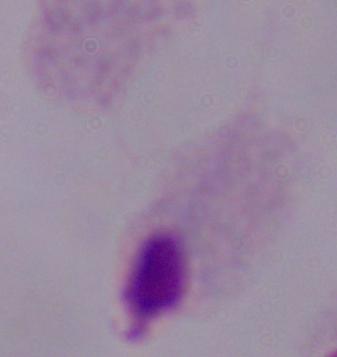
Summary:
  - Magnification: 1000x
  - Identification: trichomonad
  - Modality: photomicrograph